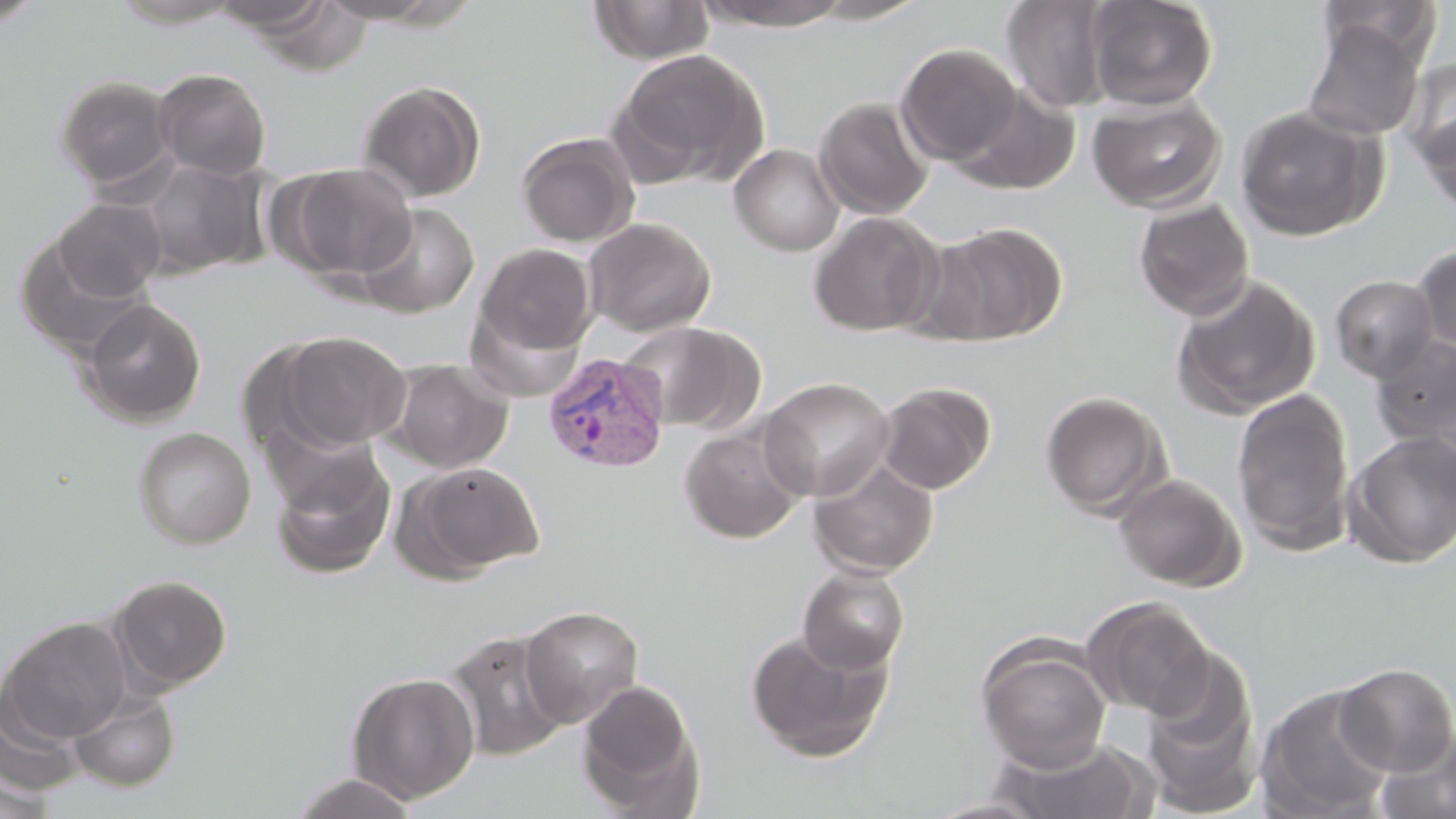

Plasmodium vivax-infected red blood cell locations = approximate bounding boxes as (x1, y1, x2, y2) in pixels: (541, 352, 671, 474)
slide-level diagnosis = Plasmodium vivax
field of view = one of a larger specimen
stain = May-Grünwald-Giemsa
modality = optical microscopy
magnification = 1000x
uninfected red blood cell locations = approximate bounding boxes as (x1, y1, x2, y2) in pixels: (108, 0, 249, 28), (314, 0, 458, 26), (696, 0, 853, 30), (1000, 0, 1116, 113), (1086, 0, 1219, 110), (0, 1, 45, 29), (207, 1, 336, 35), (587, 1, 715, 64), (806, 1, 930, 24), (1317, 1, 1442, 64), (1300, 16, 1427, 142), (895, 42, 1021, 166), (609, 49, 767, 188), (1401, 57, 1456, 169), (152, 68, 272, 180), (54, 75, 177, 191), (356, 79, 486, 202), (949, 84, 1082, 196), (1087, 92, 1226, 213), (812, 96, 934, 219), (1235, 105, 1383, 241), (1416, 111, 1456, 221), (516, 131, 640, 247), (728, 143, 845, 256), (136, 158, 270, 279), (279, 162, 417, 283), (53, 198, 166, 301), (1132, 198, 1255, 321), (354, 203, 479, 318), (807, 212, 943, 336), (582, 217, 717, 337), (922, 222, 1068, 346), (16, 237, 154, 361), (472, 243, 598, 365), (1412, 244, 1456, 357), (1170, 274, 1320, 420), (1329, 274, 1439, 382), (81, 298, 207, 427), (620, 320, 763, 434), (274, 330, 412, 454), (1370, 335, 1456, 450), (385, 358, 514, 474), (759, 376, 895, 501), (874, 382, 996, 495), (1230, 387, 1356, 555), (1040, 391, 1170, 519), (678, 423, 808, 544), (132, 426, 256, 548), (1342, 431, 1456, 568), (270, 446, 396, 579), (808, 454, 938, 579), (400, 460, 545, 579), (1112, 473, 1246, 592), (797, 565, 910, 674), (110, 574, 232, 693), (1080, 596, 1216, 719), (518, 605, 644, 728), (1, 617, 132, 744), (744, 629, 891, 762), (443, 630, 570, 760), (975, 640, 1112, 772), (1138, 651, 1261, 816), (1334, 663, 1456, 777), (345, 670, 481, 805), (576, 679, 704, 815), (1255, 685, 1395, 819), (0, 688, 84, 801), (68, 689, 180, 792), (1374, 730, 1456, 819), (988, 736, 1159, 819), (0, 766, 55, 819), (288, 773, 420, 818), (922, 797, 1051, 818)
preparation = thin blood film
image size = 1456×819 pixels